Assess this cell for malaria.
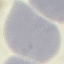
It is uninfected.

capture: smartphone camera at the microscope eyepiece
image_type: automatically extracted cell patch, resized to 64 × 64 pixels
preparation: thin blood smear
stain: Giemsa